Outline each blood parasite and name the species.
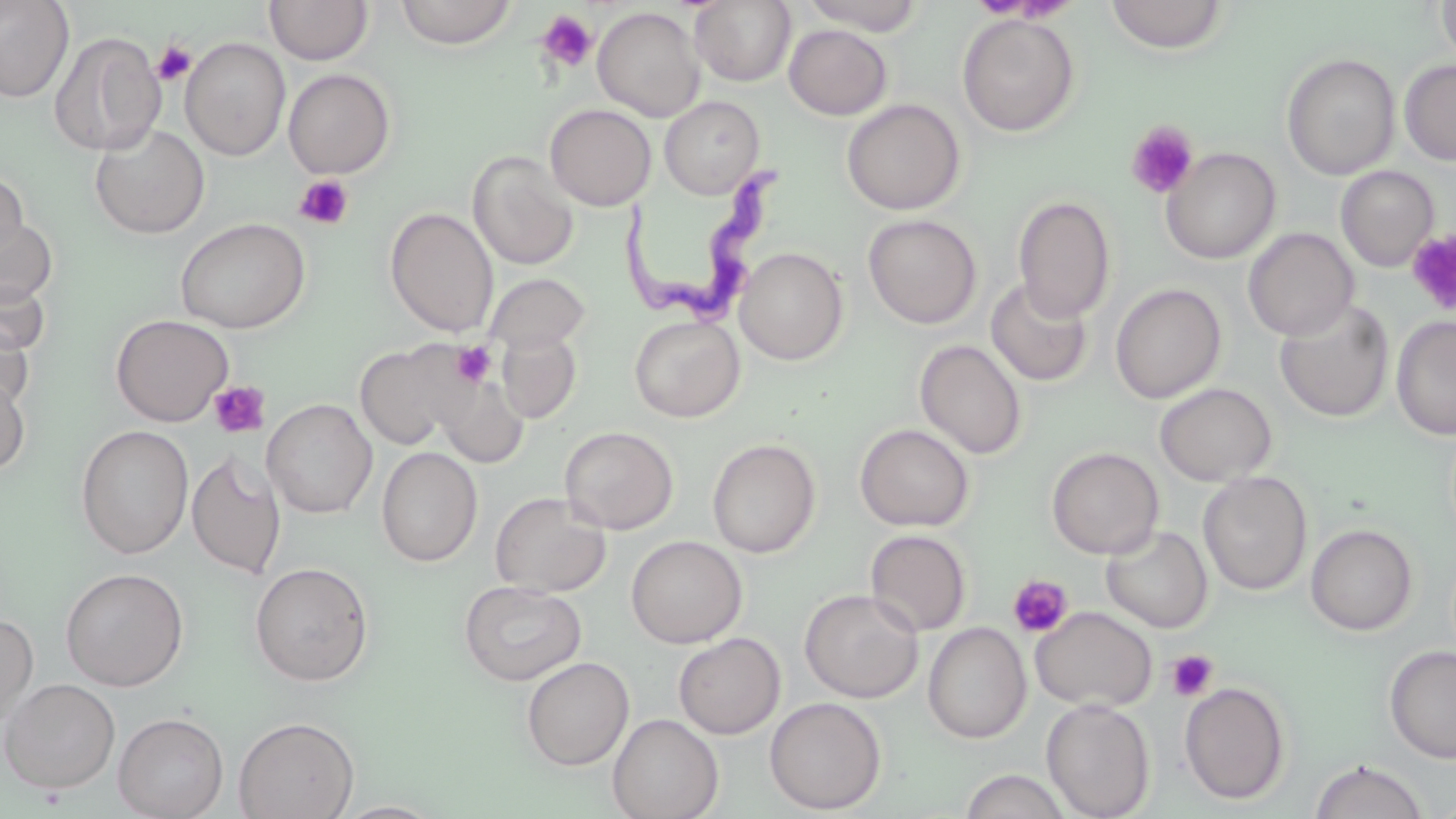

Approximate bounding boxes as (x1,y1)-(x2,y2) corner pairs in pixels.
Trypanosoma brucei: (617,157)-(798,334).
No Plasmodium falciparum, Plasmodium ovale, Plasmodium malariae, Plasmodium vivax, or Babesia divergens observed.

Summary:
  - Platelet locations: (536,10)-(599,74), (150,39)-(198,87), (1126,121)-(1199,199), (293,174)-(355,230), (1406,229)-(1456,316), (451,342)-(496,387), (209,381)-(271,440), (1007,575)-(1074,639), (1167,649)-(1219,701)
  - Uninfected red blood cell locations: (0,0)-(75,103), (264,0)-(373,65), (394,0)-(518,48), (690,0)-(797,86), (800,0)-(927,35), (1104,0)-(1230,54), (1436,0)-(1456,68), (592,6)-(706,122), (957,12)-(1080,137), (784,24)-(892,120), (48,31)-(166,157), (180,37)-(291,160), (1281,53)-(1401,180), (1399,59)-(1456,167), (283,68)-(396,179), (659,96)-(765,199), (842,98)-(966,215), (544,103)-(656,210), (89,123)-(210,238), (1161,146)-(1281,264), (469,151)-(579,270), (1335,165)-(1439,272), (0,169)-(29,266), (1012,195)-(1116,322), (385,207)-(499,337), (1,211)-(58,307), (863,214)-(982,329), (175,217)-(311,334), (1243,227)-(1359,341), (734,246)-(849,365), (483,273)-(590,356), (0,277)-(50,358), (985,277)-(1094,387), (1110,283)-(1226,403), (1274,299)-(1395,423), (111,314)-(234,426), (1391,314)-(1456,441), (629,315)-(745,422), (0,316)-(34,413), (497,329)-(581,423), (915,339)-(1027,460), (355,340)-(474,451), (0,371)-(31,476), (434,374)-(529,467), (1155,382)-(1277,486), (262,398)-(377,518), (854,422)-(974,531), (75,424)-(194,559), (559,425)-(679,534), (706,438)-(821,558), (376,446)-(483,566), (1046,446)-(1165,559), (186,451)-(287,579), (1197,470)-(1312,596), (490,491)-(611,598), (1305,523)-(1418,636), (1101,525)-(1213,633), (864,529)-(971,638), (626,535)-(747,648), (249,561)-(374,686), (60,567)-(189,691), (458,580)-(588,687), (799,588)-(923,703), (1030,606)-(1157,712), (0,613)-(38,727), (923,622)-(1032,743), (673,633)-(786,739), (1384,645)-(1456,763), (521,656)-(634,771), (0,678)-(120,795), (1179,681)-(1291,805), (764,696)-(887,815), (1041,698)-(1155,819), (113,712)-(229,819), (607,713)-(723,819), (233,716)-(359,819), (1308,758)-(1430,819), (958,769)-(1074,819), (332,801)-(445,819)
  - Slide-level diagnosis: Trypanosoma brucei
  - Image size: 1456×819 pixels
  - Preparation: thin blood smear
  - Magnification: 1000x
  - Modality: light microscopy
  - Stain: May-Grünwald-Giemsa
  - Field of view: one of a larger specimen